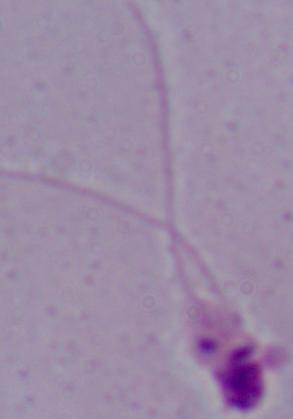

Summary:
  - Modality: micrograph
  - Magnification: 1000x
  - Identification: Leishmania